Name the parasite shown.
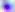
This is Toxoplasma gondii.

Photomicrograph. Captured at 400x magnification.